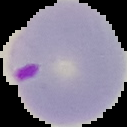

preparation = thin blood film
result = malaria parasites identified
image size = 127×127 pixels
image type = segmented cell region with the area outside set to black